Assess this cell for malaria.
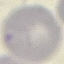

Uninfected.

preparation = thin blood film
image type = automatically extracted cell patch, resized to 64 × 64 pixels
capture = smartphone camera at the microscope eyepiece
stain = Giemsa